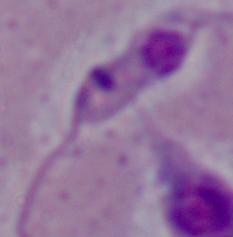

Summary:
  - Modality: micrograph
  - Identification: Leishmania
  - Magnification: 1000x